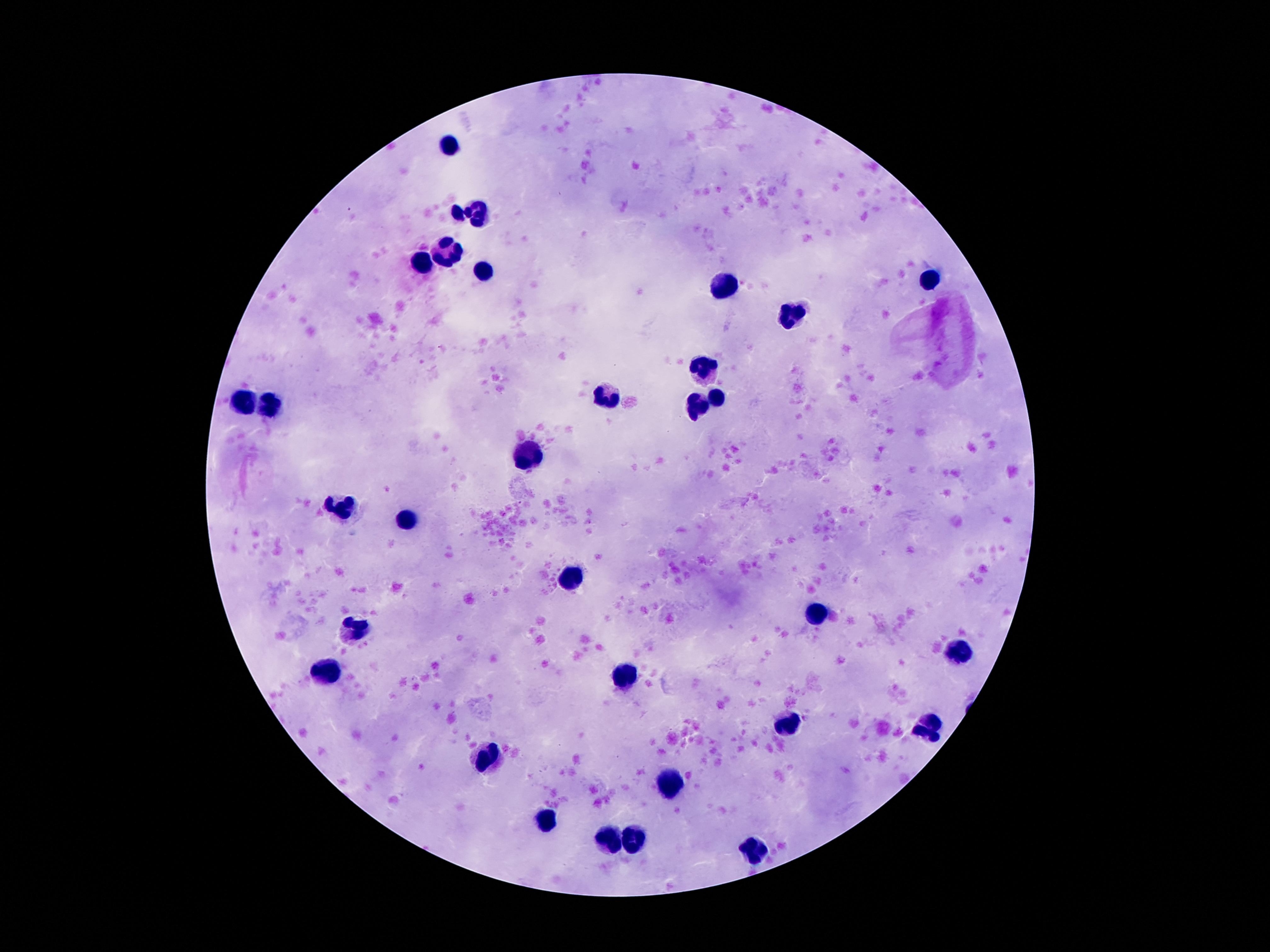
field of view = single
capture = smartphone camera through the microscope eyepiece
patient malaria status = not infected
stain = Giemsa
leukocyte locations = approximate centers as [x, y] in pixels: [447, 144], [477, 209], [456, 211], [447, 251], [422, 263], [479, 272], [934, 283], [724, 286], [793, 312], [705, 366], [607, 395], [718, 400], [273, 401], [243, 402], [697, 404], [525, 455], [340, 507], [407, 519], [569, 581], [814, 614], [353, 625], [957, 652], [325, 669], [623, 676], [791, 723], [926, 729], [487, 759], [672, 785], [548, 825], [611, 842], [636, 843], [753, 851]
magnification = 100x
image size = 1270×952 pixels
preparation = thick blood smear